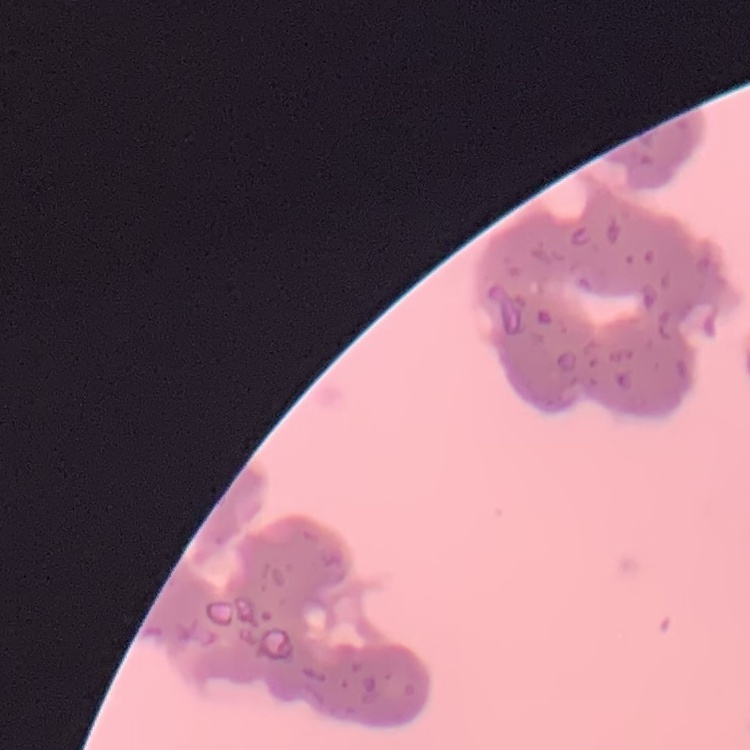
erythrocyte_morphology: rouleaux formation
stain: Field's or Giemsa
image_type: square crop of a larger photomicrograph
preparation: thin blood smear